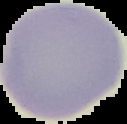
Summary:
  - Malaria status: uninfected
  - Image size: 127×124 pixels
  - Image type: segmented cell region on a black background
  - Preparation: thin blood film